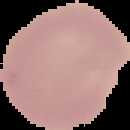
Malaria status: uninfected. The area outside the segmented cell region is set to black. Image is 130×130 pixels. From a thin blood film.